Point out each malaria parasite and each leukocyte.
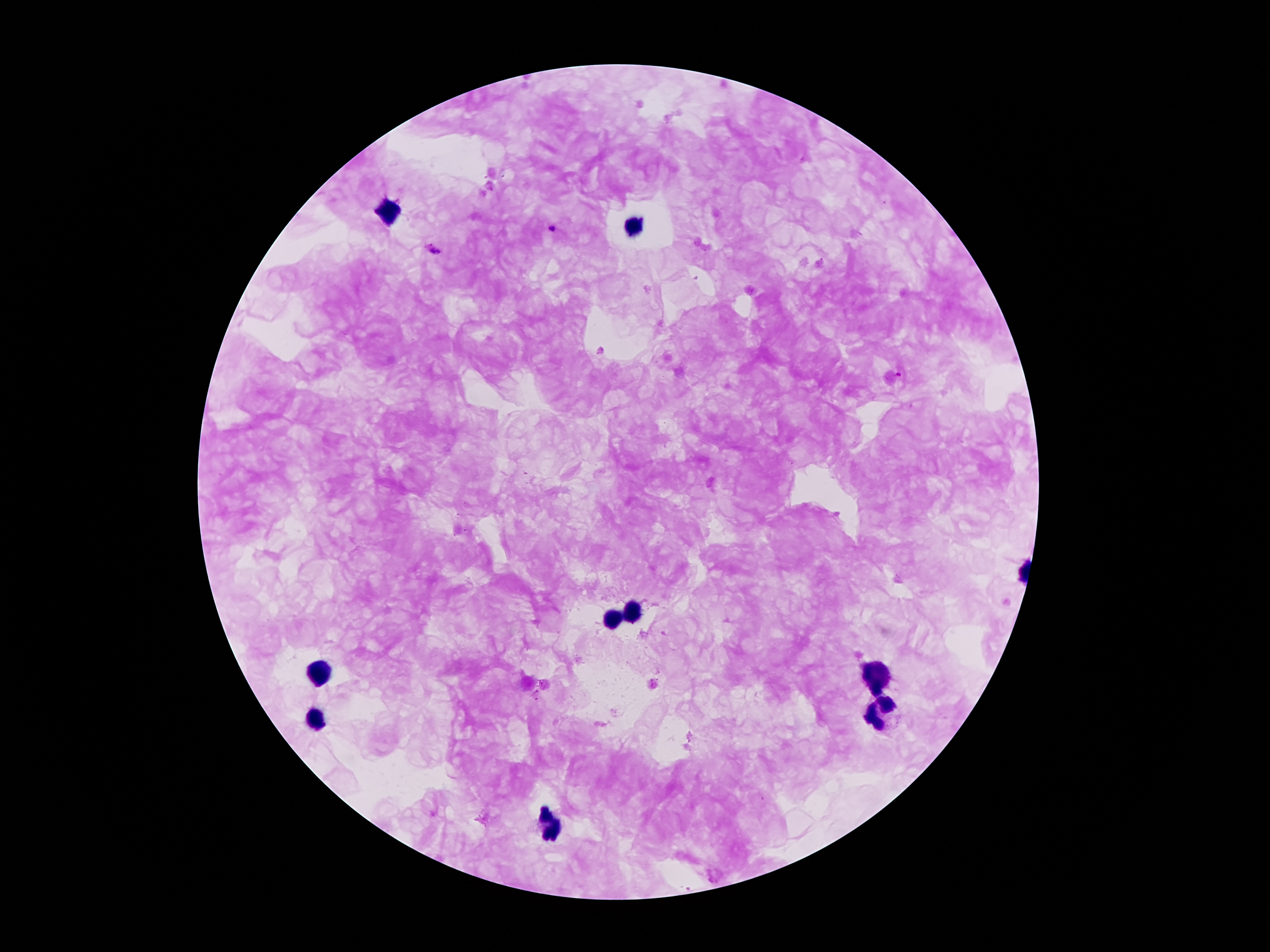
Approximate object centers, in pixels from the top-left corner.
Malaria parasites: (x=553, y=229), (x=431, y=250).
Leukocytes: (x=389, y=211), (x=635, y=230), (x=632, y=614), (x=612, y=620), (x=315, y=674), (x=874, y=677), (x=877, y=712), (x=313, y=721), (x=550, y=828).

magnification: 100x
stain: Giemsa
image_size: 1270×952 pixels
preparation: thick blood smear
patient_malaria_status: infected with Plasmodium falciparum
capture: smartphone through the microscope eyepiece
field_of_view: single